Report the malaria status of this cell.
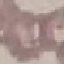

Uninfected.

{
  "image_type": "cell patch, automatically extracted from a larger field of view and resized to 64 × 64 pixels",
  "stain": "Giemsa",
  "capture": "smartphone camera at the microscope eyepiece",
  "preparation": "thin blood smear"
}